Assess this cell for malaria.
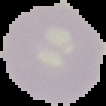

Uninfected.

image_size: 106×106 pixels
image_type: segmented cell region with the area outside set to black
preparation: thin blood smear